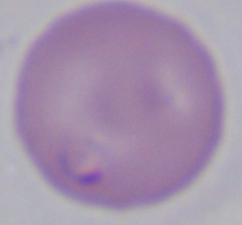

Summary:
  - Magnification: 1000x
  - Identification: Babesia
  - Modality: micrograph